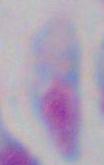

Photomicrograph. Toxoplasma gondii is shown. Captured at 1000x magnification.